Name the blood parasite species.
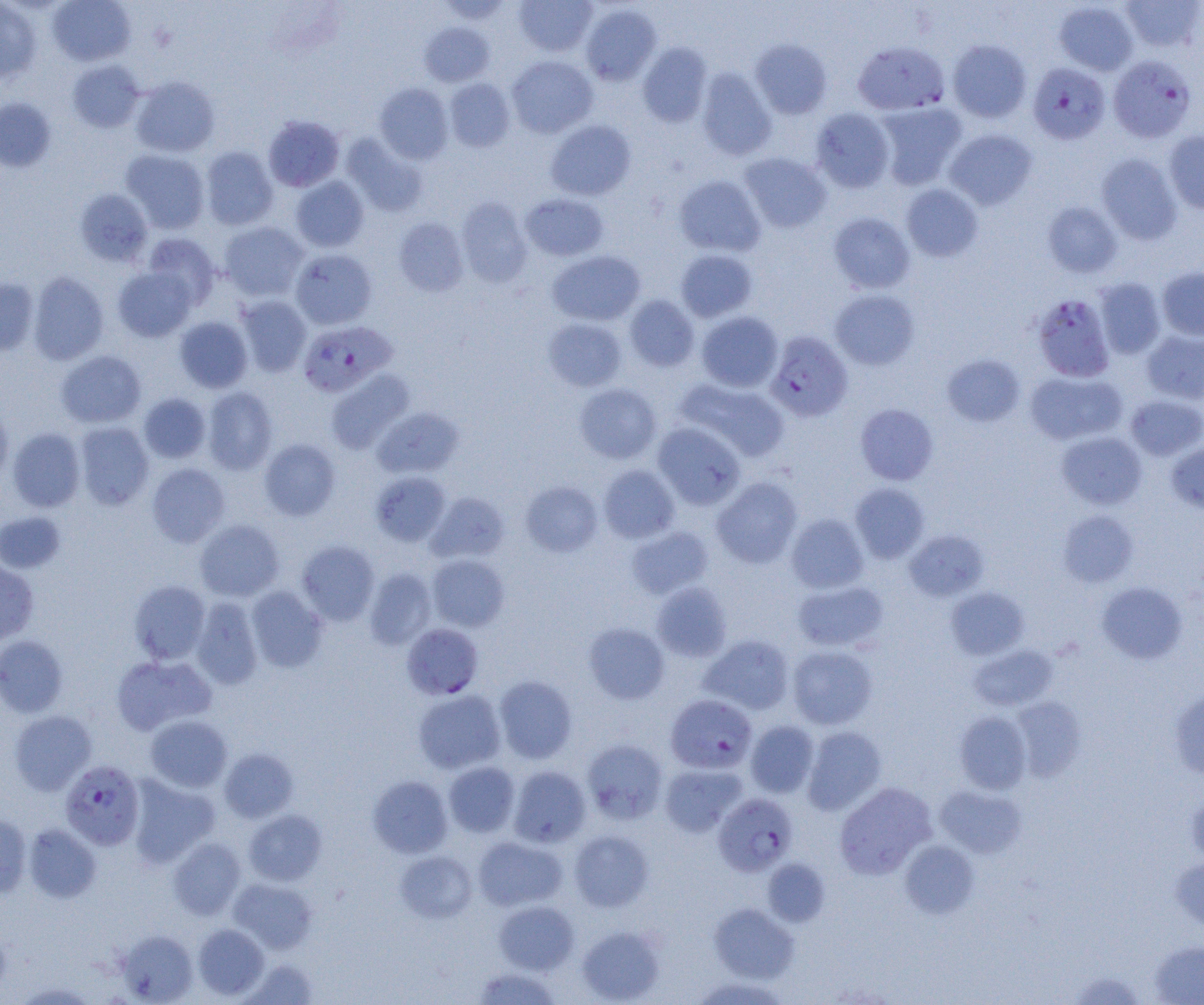

Plasmodium falciparum.

field of view = one of a larger specimen
Plasmodium falciparum-infected red blood cell locations = approximate bounding boxes as named x1/y1/x2/y2 corners in pixels: (x1=853, y1=42, x2=948, y2=115), (x1=1108, y1=55, x2=1196, y2=142), (x1=1027, y1=62, x2=1110, y2=144), (x1=1031, y1=293, x2=1115, y2=382), (x1=297, y1=321, x2=397, y2=397), (x1=765, y1=331, x2=853, y2=422), (x1=402, y1=623, x2=483, y2=699), (x1=665, y1=694, x2=757, y2=773), (x1=60, y1=759, x2=145, y2=850), (x1=713, y1=793, x2=798, y2=876)
modality = optical microscopy
magnification = 1000x
uninfected red blood cell locations = approximate bounding boxes as named x1/y1/x2/y2 corners in pixels: (x1=48, y1=0, x2=136, y2=66), (x1=435, y1=0, x2=514, y2=24), (x1=514, y1=0, x2=597, y2=56), (x1=1120, y1=0, x2=1203, y2=52), (x1=0, y1=1, x2=41, y2=82), (x1=1054, y1=1, x2=1139, y2=76), (x1=580, y1=4, x2=661, y2=85), (x1=420, y1=22, x2=495, y2=87), (x1=750, y1=39, x2=832, y2=119), (x1=948, y1=39, x2=1031, y2=123), (x1=638, y1=42, x2=712, y2=127), (x1=506, y1=56, x2=598, y2=138), (x1=67, y1=60, x2=145, y2=133), (x1=696, y1=68, x2=776, y2=161), (x1=130, y1=76, x2=220, y2=157), (x1=444, y1=78, x2=515, y2=152), (x1=375, y1=82, x2=454, y2=164), (x1=0, y1=98, x2=56, y2=172), (x1=875, y1=103, x2=967, y2=190), (x1=811, y1=108, x2=895, y2=192), (x1=263, y1=115, x2=344, y2=191), (x1=545, y1=120, x2=636, y2=201), (x1=944, y1=129, x2=1037, y2=209), (x1=1164, y1=131, x2=1204, y2=213), (x1=341, y1=133, x2=428, y2=217), (x1=200, y1=146, x2=278, y2=230), (x1=121, y1=150, x2=210, y2=234), (x1=739, y1=152, x2=832, y2=233), (x1=1096, y1=153, x2=1182, y2=245), (x1=674, y1=175, x2=766, y2=257), (x1=290, y1=176, x2=369, y2=252), (x1=901, y1=184, x2=983, y2=262), (x1=75, y1=188, x2=153, y2=268), (x1=521, y1=193, x2=608, y2=261), (x1=456, y1=196, x2=532, y2=287), (x1=1042, y1=201, x2=1122, y2=278), (x1=828, y1=212, x2=915, y2=294), (x1=394, y1=217, x2=469, y2=296), (x1=219, y1=222, x2=309, y2=301), (x1=142, y1=233, x2=221, y2=308), (x1=290, y1=249, x2=377, y2=329), (x1=675, y1=249, x2=757, y2=322), (x1=547, y1=250, x2=645, y2=326), (x1=113, y1=266, x2=197, y2=342), (x1=1157, y1=266, x2=1204, y2=340), (x1=28, y1=271, x2=109, y2=365), (x1=0, y1=277, x2=39, y2=356), (x1=1094, y1=277, x2=1166, y2=359), (x1=830, y1=289, x2=920, y2=370), (x1=624, y1=294, x2=699, y2=372), (x1=235, y1=296, x2=312, y2=377), (x1=696, y1=311, x2=783, y2=392), (x1=174, y1=316, x2=253, y2=393), (x1=543, y1=318, x2=627, y2=392), (x1=1141, y1=329, x2=1204, y2=404), (x1=55, y1=350, x2=146, y2=428), (x1=942, y1=353, x2=1025, y2=427), (x1=326, y1=370, x2=415, y2=454), (x1=1025, y1=370, x2=1127, y2=445), (x1=675, y1=378, x2=789, y2=461), (x1=574, y1=383, x2=662, y2=464), (x1=202, y1=387, x2=278, y2=475), (x1=138, y1=393, x2=211, y2=463), (x1=1125, y1=395, x2=1204, y2=461), (x1=855, y1=404, x2=938, y2=485), (x1=0, y1=405, x2=13, y2=486), (x1=372, y1=407, x2=462, y2=479), (x1=74, y1=422, x2=154, y2=510), (x1=652, y1=423, x2=746, y2=510), (x1=6, y1=427, x2=85, y2=512), (x1=1057, y1=431, x2=1147, y2=509), (x1=259, y1=439, x2=340, y2=520), (x1=1166, y1=442, x2=1204, y2=515), (x1=146, y1=463, x2=230, y2=547), (x1=598, y1=465, x2=680, y2=543), (x1=370, y1=471, x2=451, y2=546), (x1=711, y1=477, x2=802, y2=568), (x1=521, y1=481, x2=603, y2=557), (x1=850, y1=482, x2=929, y2=563), (x1=426, y1=492, x2=509, y2=564), (x1=1058, y1=510, x2=1139, y2=587), (x1=0, y1=512, x2=66, y2=573), (x1=786, y1=513, x2=868, y2=594), (x1=195, y1=519, x2=284, y2=602), (x1=626, y1=525, x2=714, y2=599), (x1=904, y1=530, x2=989, y2=601), (x1=297, y1=540, x2=380, y2=625), (x1=426, y1=554, x2=509, y2=632), (x1=0, y1=561, x2=39, y2=645), (x1=364, y1=568, x2=437, y2=650), (x1=129, y1=580, x2=210, y2=664), (x1=793, y1=580, x2=888, y2=652), (x1=652, y1=582, x2=731, y2=661), (x1=1096, y1=582, x2=1187, y2=663), (x1=246, y1=586, x2=328, y2=672), (x1=946, y1=587, x2=1029, y2=660), (x1=190, y1=597, x2=263, y2=689), (x1=584, y1=623, x2=670, y2=703), (x1=0, y1=635, x2=68, y2=718), (x1=699, y1=635, x2=794, y2=714), (x1=968, y1=644, x2=1058, y2=711), (x1=787, y1=646, x2=877, y2=730), (x1=111, y1=654, x2=216, y2=735), (x1=494, y1=675, x2=577, y2=764), (x1=1168, y1=688, x2=1204, y2=779), (x1=413, y1=689, x2=506, y2=774), (x1=1011, y1=697, x2=1086, y2=781), (x1=9, y1=710, x2=96, y2=795), (x1=955, y1=711, x2=1032, y2=794), (x1=145, y1=714, x2=233, y2=792), (x1=745, y1=721, x2=819, y2=797), (x1=802, y1=726, x2=886, y2=815), (x1=582, y1=739, x2=668, y2=824), (x1=219, y1=748, x2=298, y2=822), (x1=443, y1=762, x2=520, y2=837), (x1=660, y1=763, x2=746, y2=836), (x1=508, y1=765, x2=591, y2=847), (x1=127, y1=775, x2=220, y2=867), (x1=367, y1=775, x2=453, y2=858), (x1=834, y1=782, x2=936, y2=879), (x1=935, y1=785, x2=1027, y2=858), (x1=1185, y1=791, x2=1204, y2=868), (x1=243, y1=810, x2=327, y2=886), (x1=0, y1=814, x2=32, y2=898), (x1=23, y1=823, x2=101, y2=903), (x1=569, y1=829, x2=654, y2=911), (x1=473, y1=836, x2=567, y2=911), (x1=168, y1=837, x2=246, y2=920), (x1=900, y1=840, x2=979, y2=918), (x1=395, y1=850, x2=477, y2=923), (x1=763, y1=858, x2=830, y2=926), (x1=1170, y1=858, x2=1204, y2=933), (x1=228, y1=878, x2=317, y2=953), (x1=494, y1=900, x2=579, y2=974), (x1=708, y1=902, x2=799, y2=983), (x1=192, y1=923, x2=269, y2=1000), (x1=576, y1=925, x2=665, y2=1003), (x1=0, y1=927, x2=10, y2=996), (x1=116, y1=929, x2=198, y2=1004), (x1=1149, y1=940, x2=1204, y2=1004), (x1=240, y1=958, x2=319, y2=1004), (x1=473, y1=967, x2=561, y2=1004), (x1=1067, y1=971, x2=1148, y2=1004), (x1=690, y1=975, x2=791, y2=1005), (x1=11, y1=982, x2=99, y2=1004)
preparation = thin blood film
image size = 1204×1005 pixels